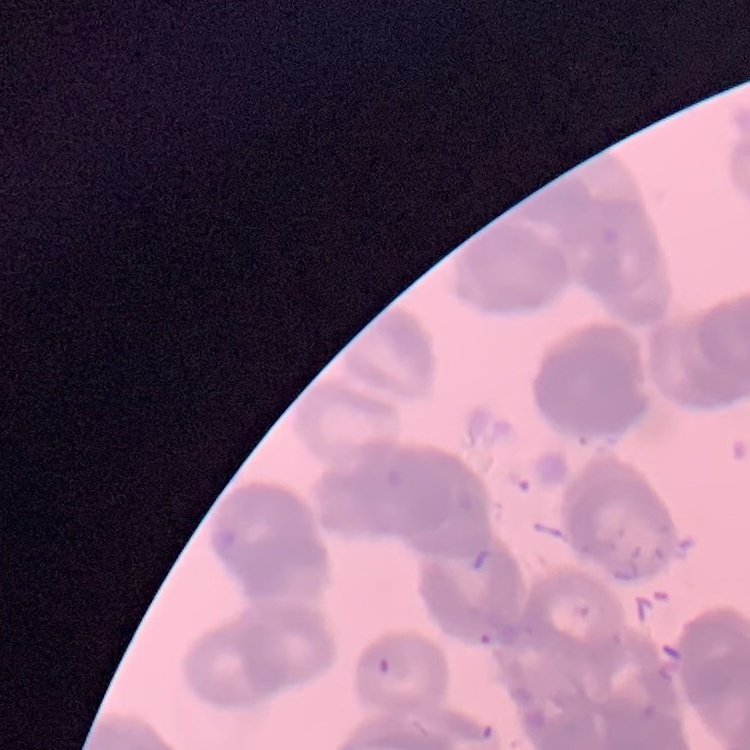 The red blood cells show rouleaux formation. Stained with either Field's or Giemsa. One tile cut from a larger photomicrograph. Thin blood smear.